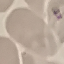

Summary:
  - Result: no malaria parasites detected
  - Capture: smartphone through the microscope eyepiece
  - Preparation: thin blood film
  - Stain: Giemsa
  - Image type: cell patch, automatically extracted from a larger field of view and resized to 64 × 64 pixels